Locate every leukocyte (white blood cell).
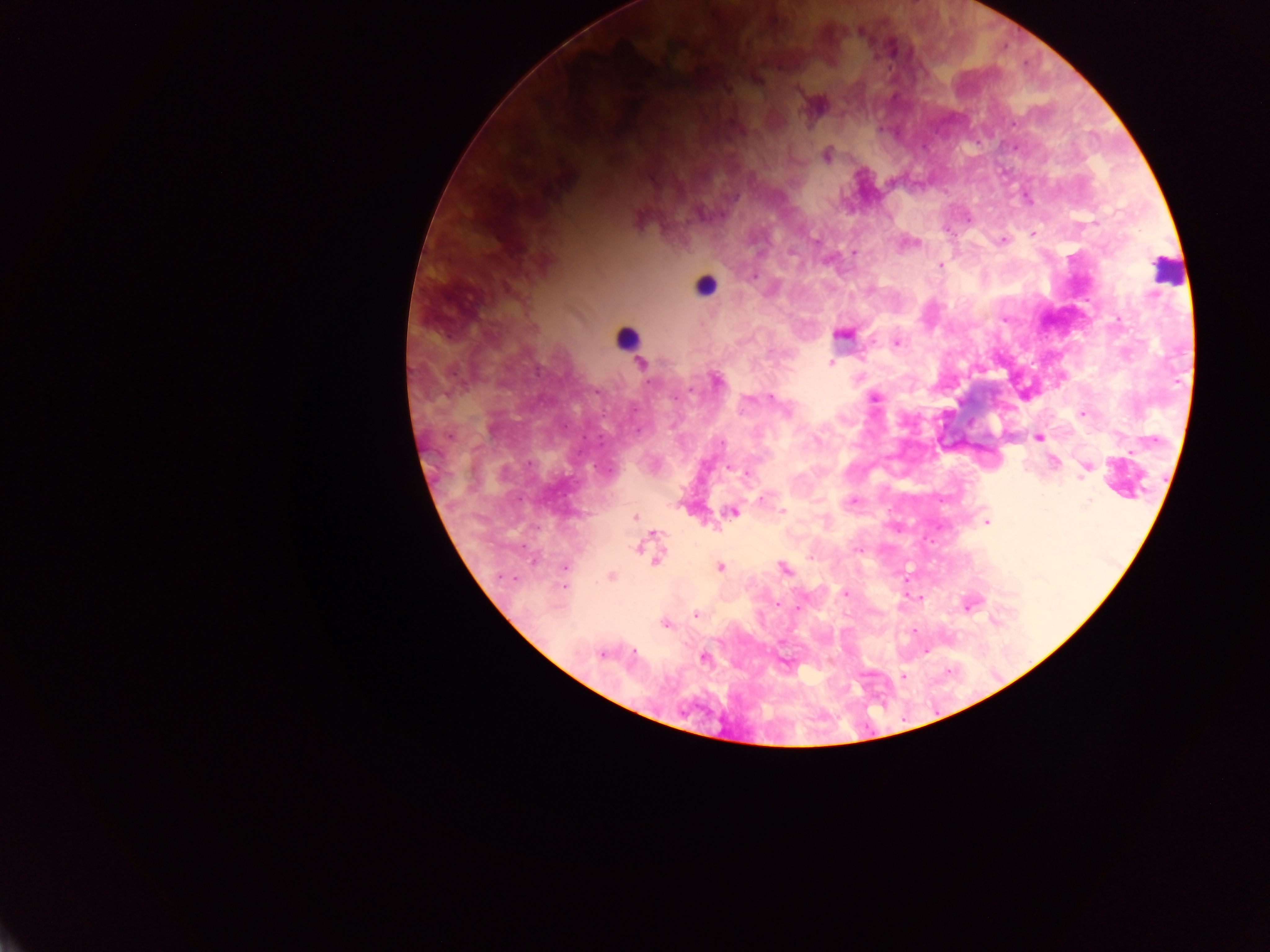
Approximate centers as x y in pixels.
Leukocytes: 1166 273; 707 291; 634 341.

Summary:
  - Malaria parasite locations: 1025 65; 1015 123; 979 143; 1027 197; 968 220; 1034 233; 1002 242; 940 265; 897 342; 829 361; 647 383; 675 398; 875 398; 635 410; 1081 414; 602 416; 584 437; 529 464; 1087 464; 595 467; 1079 479; 941 501; 1087 502; 783 510; 987 521; 537 529; 898 531; 523 546; 855 551; 720 566; 564 569; 515 578; 906 581; 563 587; 845 591; 922 601; 777 605; 966 607; 799 609; 693 614; 993 618; 665 623; 913 632; 600 656; 702 657; 786 663; 831 663; 949 671; 904 678
  - Preparation: thick blood film
  - Image size: 1270×952 pixels
  - Country: Ghana
  - Field of view: single
  - Capture: mobile-phone photograph through a microscope